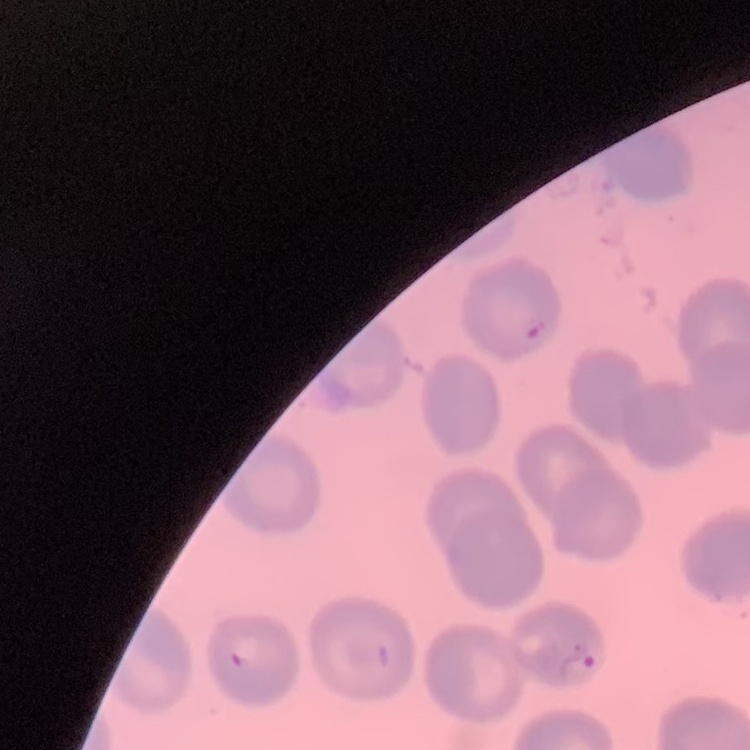 The red blood cells show no rouleaux formation. Thin blood smear. Square crop of a larger photomicrograph. Stained with either Field's or Giemsa.